Give the extent of all Plasmodium ovale-infected red blood cells.
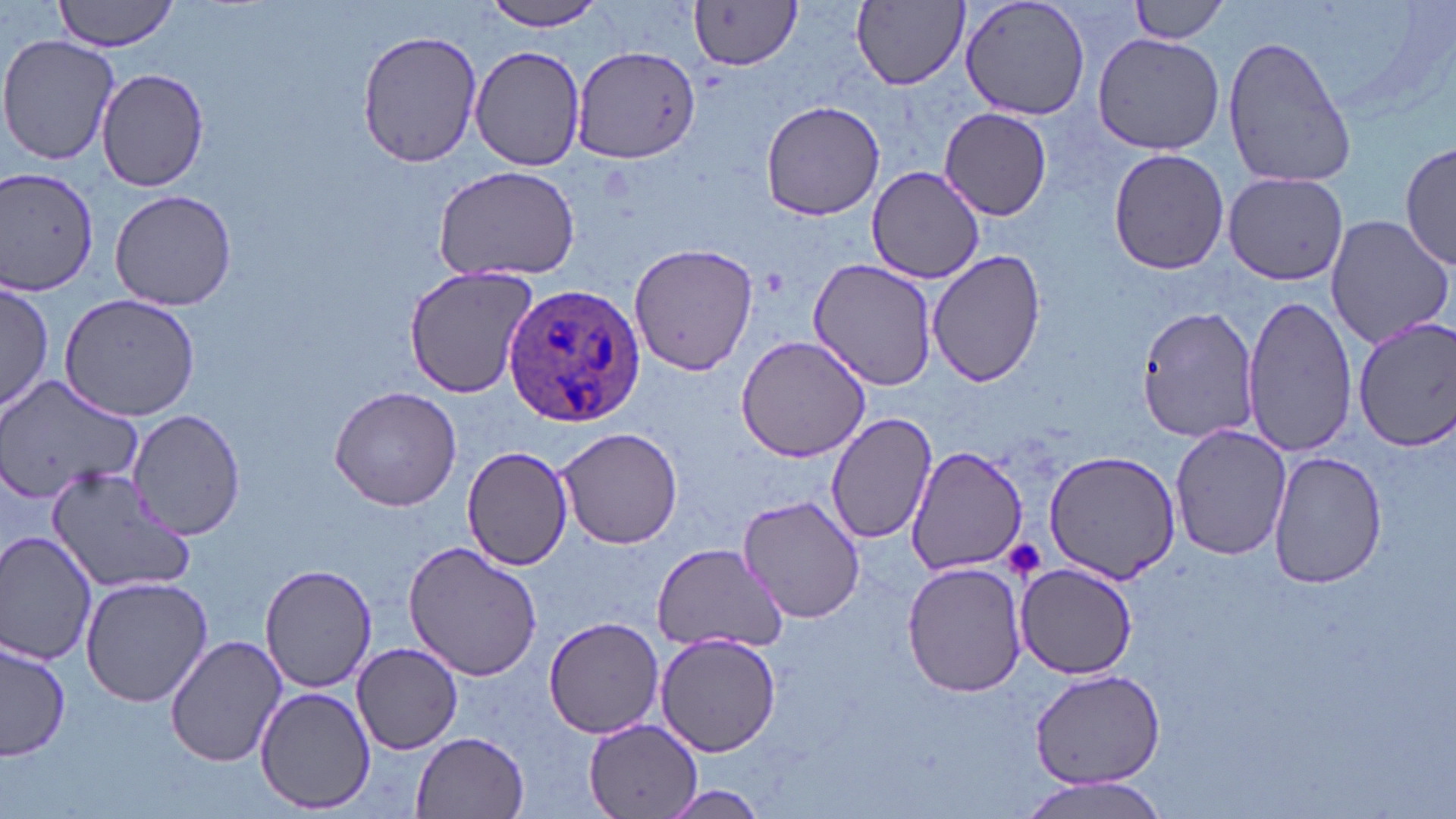
Approximate bounding boxes as named x1/y1/x2/y2 corners in pixels.
Plasmodium ovale-infected red blood cells: (x1=503, y1=285, x2=646, y2=427).

Uninfected red blood cell locations: (x1=53, y1=0, x2=183, y2=53), (x1=849, y1=0, x2=972, y2=92), (x1=959, y1=0, x2=1094, y2=121), (x1=1128, y1=0, x2=1233, y2=44), (x1=475, y1=2, x2=614, y2=31), (x1=690, y1=4, x2=800, y2=70), (x1=355, y1=26, x2=481, y2=170), (x1=1092, y1=31, x2=1223, y2=156), (x1=0, y1=34, x2=120, y2=167), (x1=1221, y1=35, x2=1357, y2=189), (x1=571, y1=45, x2=699, y2=164), (x1=470, y1=46, x2=587, y2=172), (x1=95, y1=66, x2=211, y2=192), (x1=759, y1=99, x2=886, y2=221), (x1=939, y1=108, x2=1053, y2=219), (x1=1401, y1=139, x2=1454, y2=274), (x1=1108, y1=148, x2=1230, y2=276), (x1=0, y1=165, x2=102, y2=295), (x1=431, y1=165, x2=581, y2=282), (x1=867, y1=166, x2=987, y2=282), (x1=1223, y1=172, x2=1350, y2=284), (x1=109, y1=188, x2=237, y2=312), (x1=1324, y1=214, x2=1454, y2=351), (x1=628, y1=241, x2=759, y2=376), (x1=928, y1=248, x2=1047, y2=388), (x1=808, y1=259, x2=936, y2=392), (x1=402, y1=265, x2=538, y2=397), (x1=0, y1=280, x2=54, y2=417), (x1=59, y1=292, x2=201, y2=422), (x1=1242, y1=293, x2=1359, y2=460), (x1=1134, y1=305, x2=1261, y2=444), (x1=1355, y1=316, x2=1455, y2=453), (x1=736, y1=335, x2=875, y2=462), (x1=0, y1=374, x2=142, y2=506), (x1=329, y1=384, x2=461, y2=513), (x1=127, y1=409, x2=247, y2=541), (x1=826, y1=411, x2=938, y2=544), (x1=1171, y1=424, x2=1290, y2=561), (x1=556, y1=426, x2=687, y2=549), (x1=462, y1=443, x2=573, y2=571), (x1=907, y1=446, x2=1030, y2=575), (x1=1044, y1=450, x2=1181, y2=584), (x1=1269, y1=453, x2=1385, y2=588), (x1=48, y1=464, x2=197, y2=595), (x1=737, y1=494, x2=868, y2=625), (x1=0, y1=529, x2=98, y2=669), (x1=403, y1=542, x2=545, y2=682), (x1=650, y1=543, x2=787, y2=656), (x1=902, y1=561, x2=1027, y2=697), (x1=260, y1=563, x2=376, y2=693), (x1=1017, y1=564, x2=1139, y2=678), (x1=80, y1=576, x2=213, y2=707), (x1=542, y1=616, x2=666, y2=738), (x1=656, y1=633, x2=782, y2=756), (x1=165, y1=635, x2=288, y2=765), (x1=0, y1=639, x2=72, y2=765), (x1=353, y1=642, x2=463, y2=754), (x1=1027, y1=671, x2=1168, y2=789), (x1=254, y1=685, x2=377, y2=813), (x1=582, y1=717, x2=704, y2=819), (x1=412, y1=731, x2=530, y2=818), (x1=1015, y1=777, x2=1170, y2=818), (x1=649, y1=785, x2=773, y2=817). Platelet locations: (x1=1003, y1=541, x2=1047, y2=582). Slide-level diagnosis: Plasmodium ovale. Light microscopy. Thin blood smear. Captured at 1000x magnification. Single field of view. Image is 1456×819 pixels. May-Grünwald-Giemsa stain.